Classify this cell by malaria status.
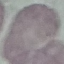
It is uninfected.

Summary:
  - Preparation: thin blood film
  - Capture: smartphone camera at the microscope eyepiece
  - Image type: automatically extracted cell patch, resized to 64 × 64 pixels
  - Stain: Giemsa